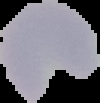

Summary:
  - Result: malaria parasites detected
  - Preparation: thin blood smear
  - Image type: cell region segmented out of the field of view; surrounding area masked to black
  - Image size: 100×103 pixels